Assess the morphology of the red blood cells.
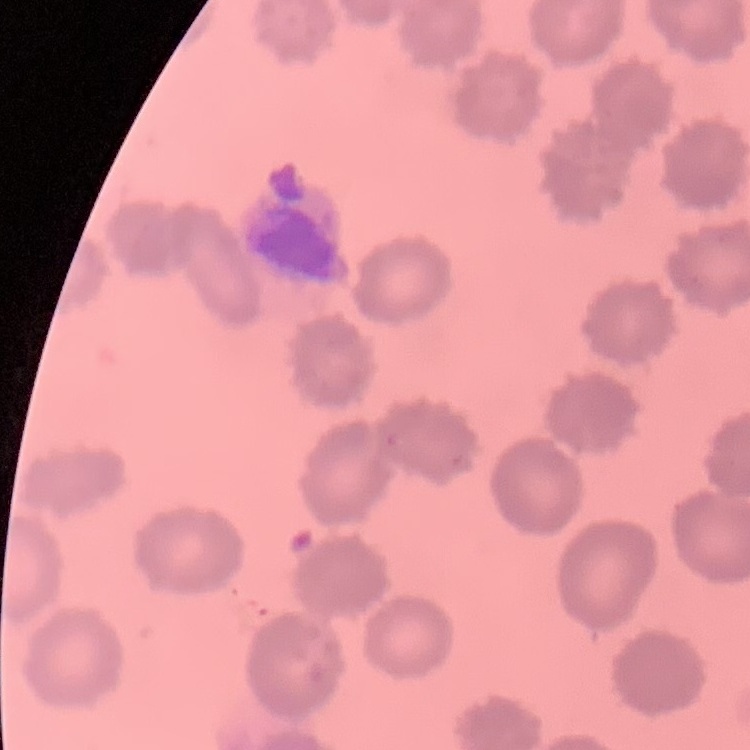
No rouleaux formation.

preparation: thin blood film
image_type: one tile cut from a larger photomicrograph
stain: Field's or Giemsa